Point out each Plasmodium parasite.
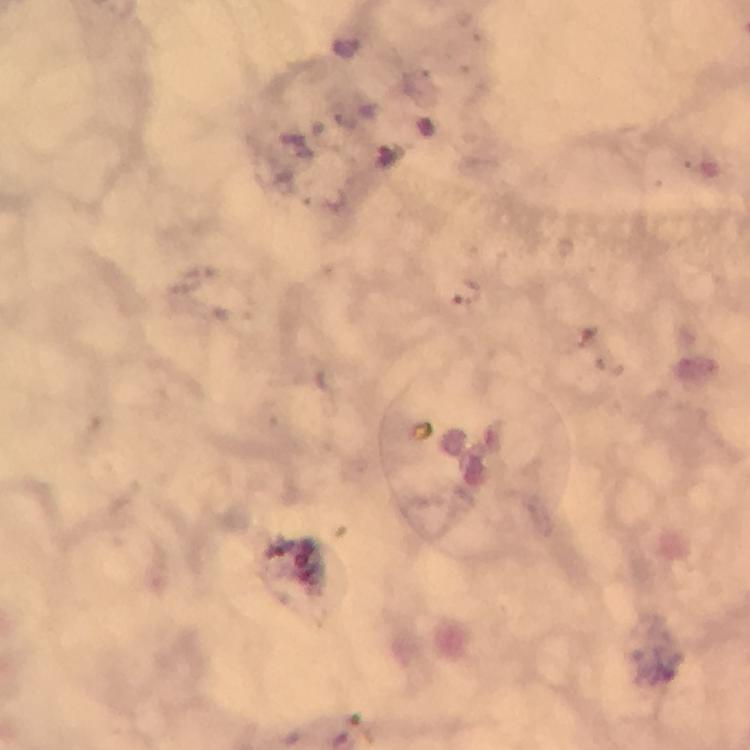

Approximate centers as [x, y] in pixels.
Plasmodium parasites: [567, 247].

100x magnification. Image is 750×750 pixels. Thick blood smear. Cropped region of a single field of view. Giemsa stain. Photographed through the microscope with a smartphone camera. From a malaria diagnostic workup. Immersion oil was used.